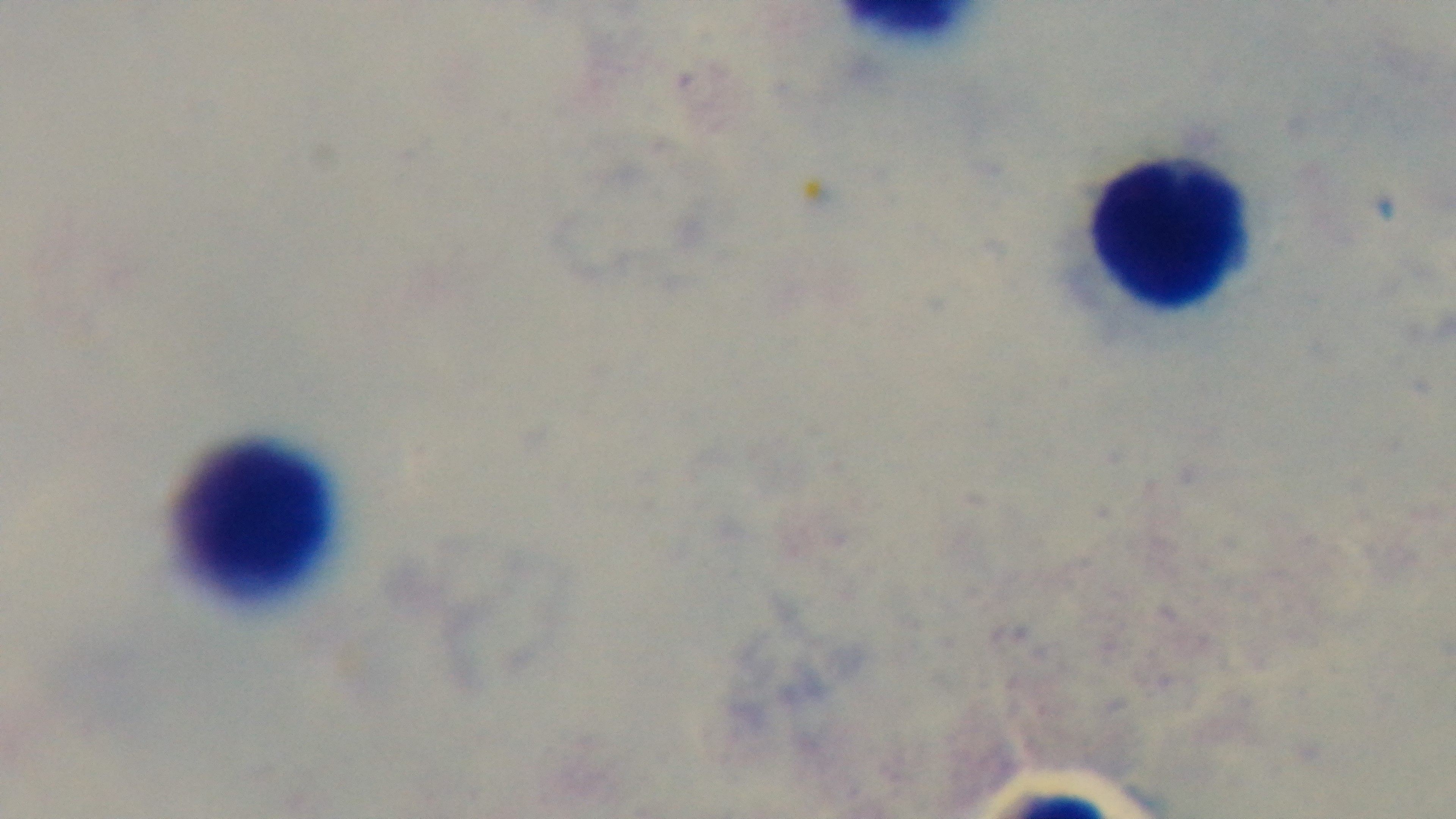
Oil-immersion objective, 100x. Mounted 4K digital camera. One field from the slide. Malaria status: uninfected. Preparation: thick blood film. Giemsa stain. Light microscopy.